Report the malaria status of this cell.
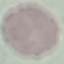
Uninfected.

Thin blood smear. Acquired by smartphone through the microscope eyepiece. Giemsa stain. Cell patch, automatically extracted from a larger field of view and resized to 64 × 64 pixels.